Outline every artifact (stain precipitate or debris).
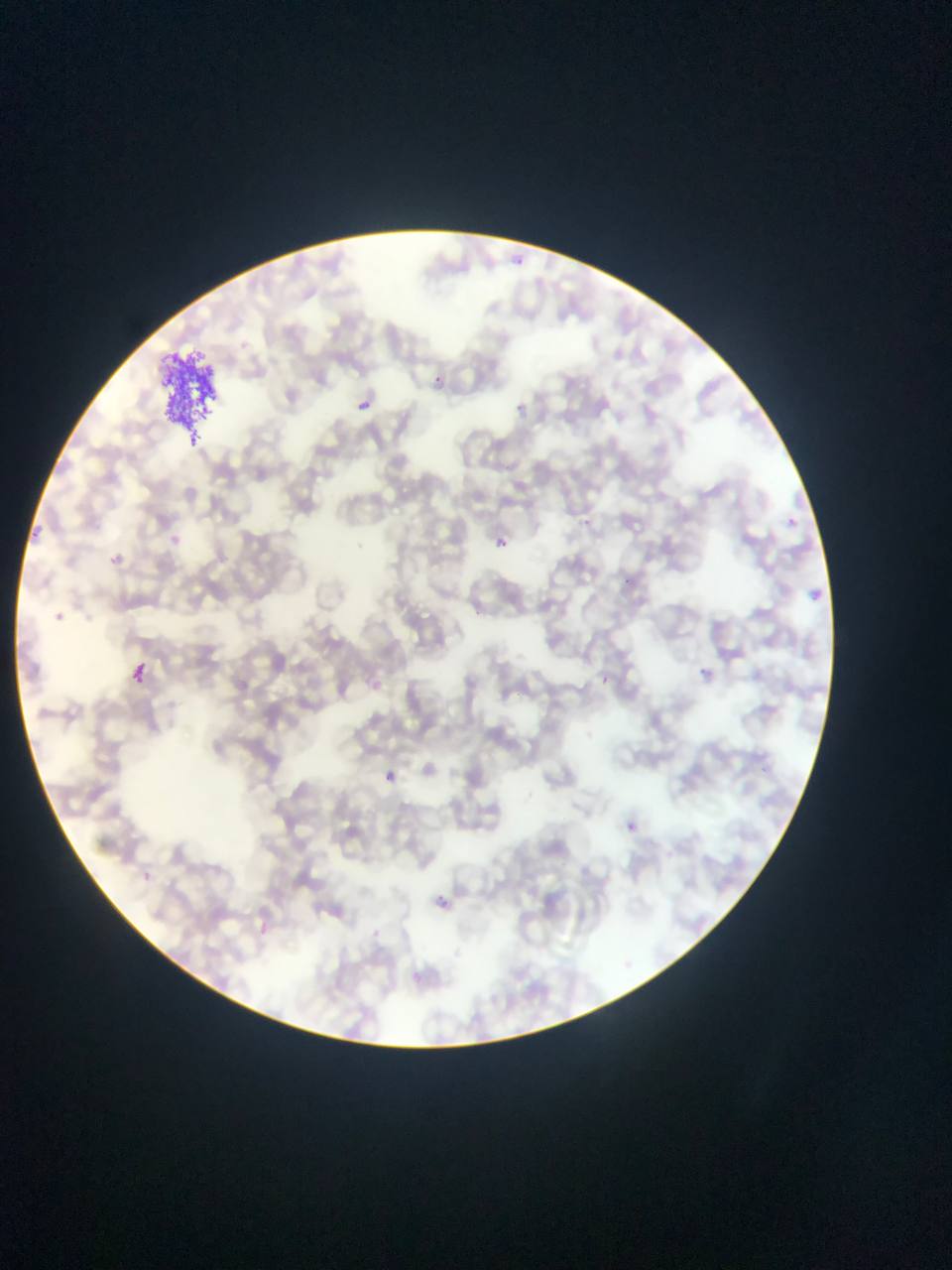
Approximate bounding boxes as left top right bottom in pixels.
Artifacts (stain precipitate or debris): 159 351 223 448.

{
  "preparation": "thin blood film",
  "image_size": "952×1270 pixels",
  "capture": "mobile-phone photograph through a microscope",
  "malaria_parasite_locations": "approximate bounding boxes as left top right bottom in pixels: 428 369 445 390; 355 393 372 416; 790 516 803 530; 495 534 509 549; 100 550 128 566; 131 655 154 680; 701 668 711 678; 385 771 397 783; 626 822 637 834",
  "country": "Ghana",
  "field_of_view": "single"
}